State which parasite is depicted.
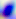

Toxoplasma gondii.

Summary:
  - Modality: photomicrograph
  - Magnification: 400x